Report the malaria status of this cell.
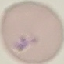

It is parasitized.

Cell patch, automatically extracted from a larger field of view and resized to 64 × 64 pixels. Giemsa stain. Acquired by smartphone through the microscope eyepiece. Thin blood film.